Locate and identify every blood parasite.
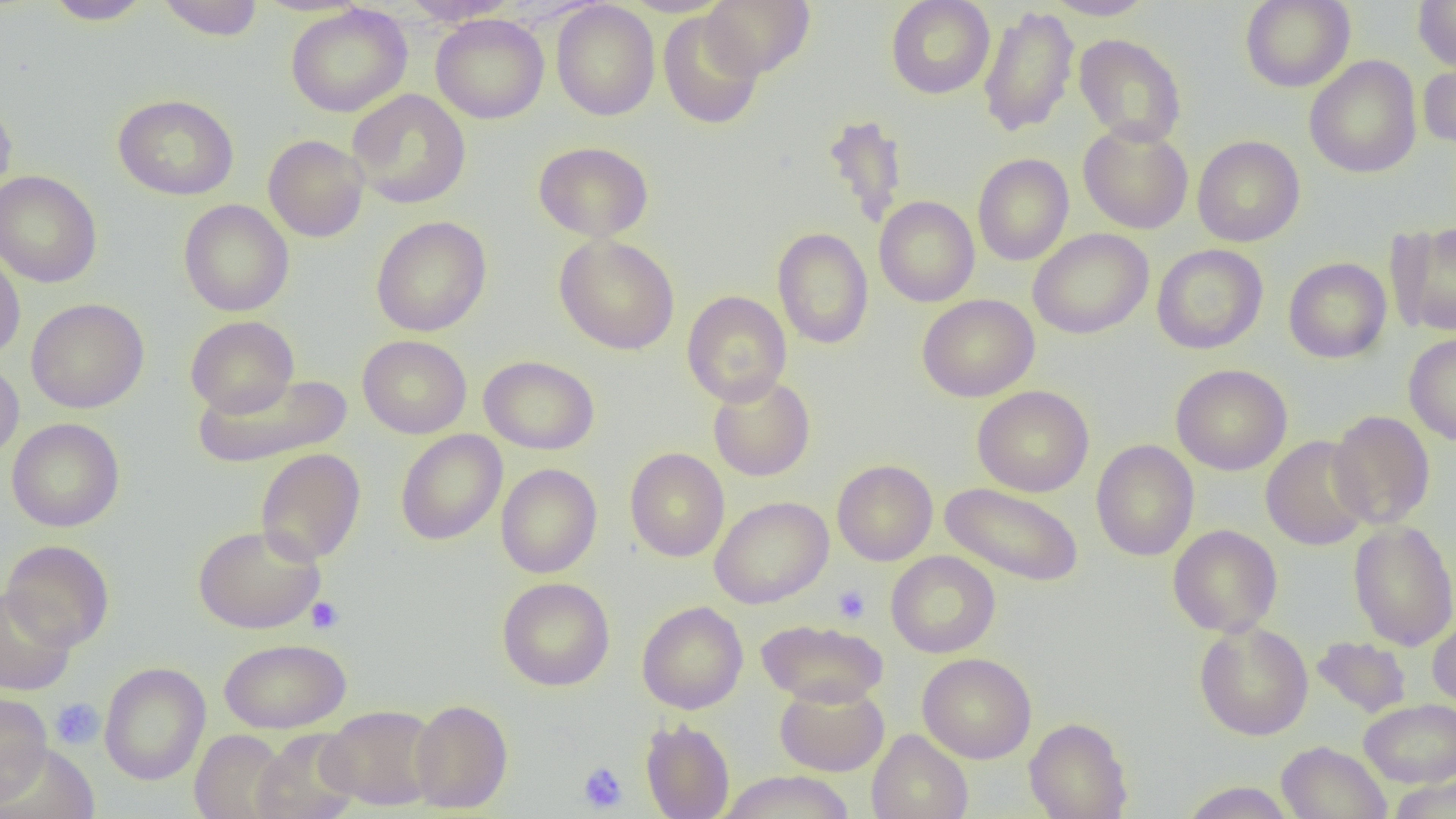

No blood parasites observed.

Approximate bounding boxes as named x1/y1/x2/y2 corners in pixels. Uninfected red blood cell locations: (x1=43, y1=0, x2=154, y2=25), (x1=156, y1=0, x2=264, y2=41), (x1=401, y1=0, x2=519, y2=26), (x1=701, y1=0, x2=814, y2=78), (x1=885, y1=0, x2=995, y2=99), (x1=1043, y1=0, x2=1156, y2=20), (x1=1240, y1=0, x2=1355, y2=92), (x1=1413, y1=0, x2=1456, y2=71), (x1=550, y1=1, x2=660, y2=121), (x1=286, y1=4, x2=412, y2=117), (x1=978, y1=6, x2=1080, y2=138), (x1=658, y1=11, x2=764, y2=130), (x1=431, y1=14, x2=549, y2=124), (x1=1074, y1=33, x2=1187, y2=146), (x1=1304, y1=55, x2=1422, y2=178), (x1=1418, y1=59, x2=1456, y2=150), (x1=348, y1=89, x2=471, y2=209), (x1=113, y1=94, x2=239, y2=200), (x1=0, y1=96, x2=17, y2=201), (x1=821, y1=113, x2=909, y2=229), (x1=1078, y1=123, x2=1193, y2=234), (x1=263, y1=134, x2=369, y2=242), (x1=1192, y1=135, x2=1305, y2=247), (x1=533, y1=141, x2=653, y2=242), (x1=972, y1=153, x2=1074, y2=266), (x1=0, y1=170, x2=102, y2=287), (x1=874, y1=196, x2=979, y2=307), (x1=178, y1=199, x2=294, y2=316), (x1=370, y1=216, x2=492, y2=336), (x1=1386, y1=221, x2=1456, y2=337), (x1=772, y1=227, x2=873, y2=349), (x1=1028, y1=228, x2=1153, y2=339), (x1=554, y1=233, x2=680, y2=355), (x1=1152, y1=244, x2=1268, y2=354), (x1=0, y1=248, x2=26, y2=363), (x1=1283, y1=257, x2=1392, y2=363), (x1=682, y1=290, x2=792, y2=406), (x1=917, y1=294, x2=1040, y2=402), (x1=26, y1=297, x2=149, y2=413), (x1=185, y1=315, x2=299, y2=417), (x1=1403, y1=332, x2=1456, y2=446), (x1=358, y1=334, x2=472, y2=438), (x1=479, y1=355, x2=599, y2=454), (x1=0, y1=359, x2=24, y2=463), (x1=1171, y1=364, x2=1293, y2=476), (x1=191, y1=373, x2=353, y2=468), (x1=708, y1=373, x2=816, y2=482), (x1=972, y1=385, x2=1094, y2=497), (x1=1328, y1=410, x2=1435, y2=530), (x1=7, y1=418, x2=125, y2=532), (x1=395, y1=430, x2=507, y2=545), (x1=1261, y1=435, x2=1373, y2=551), (x1=1092, y1=440, x2=1199, y2=561), (x1=624, y1=447, x2=729, y2=562), (x1=255, y1=448, x2=366, y2=566), (x1=832, y1=459, x2=938, y2=565), (x1=496, y1=463, x2=602, y2=578), (x1=940, y1=482, x2=1085, y2=587), (x1=710, y1=496, x2=834, y2=608), (x1=1348, y1=520, x2=1456, y2=651), (x1=193, y1=524, x2=326, y2=634), (x1=1167, y1=524, x2=1282, y2=637), (x1=1, y1=540, x2=115, y2=651), (x1=886, y1=551, x2=1000, y2=658), (x1=497, y1=577, x2=615, y2=691), (x1=0, y1=585, x2=75, y2=696), (x1=637, y1=600, x2=748, y2=714), (x1=1428, y1=615, x2=1456, y2=712), (x1=757, y1=618, x2=888, y2=708), (x1=1194, y1=620, x2=1313, y2=741), (x1=1312, y1=636, x2=1412, y2=718), (x1=219, y1=638, x2=351, y2=733), (x1=917, y1=653, x2=1037, y2=763), (x1=99, y1=661, x2=211, y2=785), (x1=775, y1=683, x2=889, y2=776), (x1=0, y1=691, x2=52, y2=803), (x1=1359, y1=698, x2=1456, y2=787), (x1=409, y1=699, x2=513, y2=813), (x1=321, y1=705, x2=439, y2=810), (x1=1024, y1=716, x2=1133, y2=819), (x1=640, y1=719, x2=735, y2=819), (x1=190, y1=729, x2=290, y2=819), (x1=251, y1=729, x2=360, y2=819), (x1=866, y1=729, x2=973, y2=819), (x1=0, y1=741, x2=100, y2=819), (x1=1276, y1=741, x2=1391, y2=819), (x1=718, y1=770, x2=854, y2=819), (x1=1388, y1=776, x2=1456, y2=819), (x1=1179, y1=781, x2=1296, y2=818). Platelet locations: (x1=832, y1=584, x2=871, y2=624), (x1=306, y1=597, x2=345, y2=634), (x1=50, y1=697, x2=104, y2=749), (x1=577, y1=761, x2=628, y2=813). Slide-level diagnosis: no evidence of blood parasites. Thin blood smear. One field of a larger specimen. Image is 1456×819 pixels. Optical microscopy. 1000x magnification.